Locate every blood parasite and identify its species.
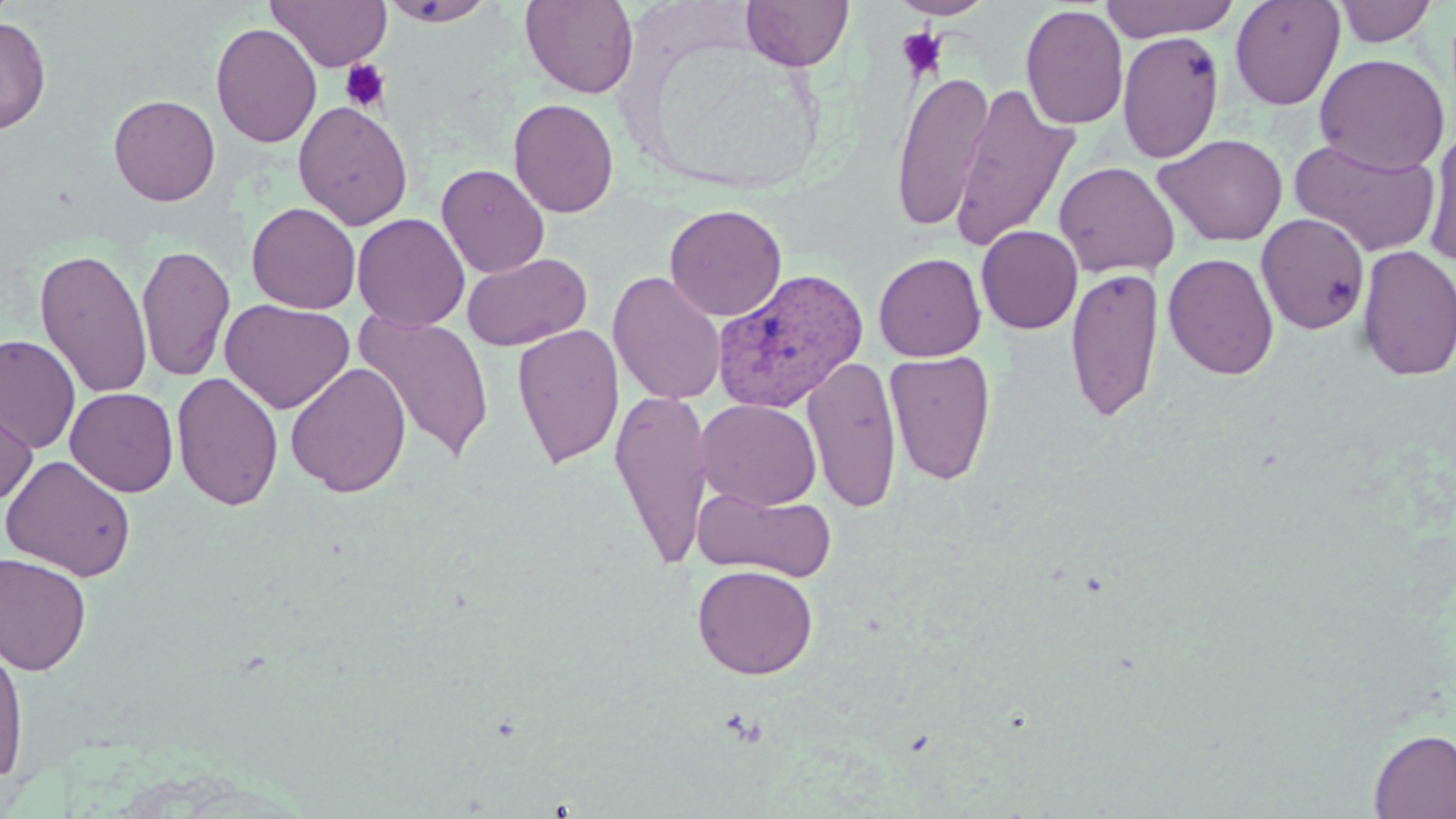

Approximate bounding boxes as (x1, y1, x2, y2) in pixels.
Plasmodium vivax-infected red blood cells: (713, 268, 869, 413).
No Plasmodium falciparum, Plasmodium ovale, Plasmodium malariae, Babesia divergens, or Trypanosoma brucei observed.

Summary:
  - Platelet locations: (897, 28, 947, 80), (339, 59, 390, 113)
  - Uninfected red blood cell locations: (378, 0, 497, 26), (520, 0, 639, 98), (741, 0, 853, 71), (890, 0, 995, 20), (1099, 0, 1241, 42), (1230, 0, 1345, 110), (1333, 0, 1439, 47), (267, 1, 391, 71), (1020, 4, 1129, 130), (0, 15, 51, 135), (210, 22, 322, 148), (1116, 30, 1225, 164), (1314, 53, 1450, 175), (890, 70, 994, 231), (948, 83, 1080, 251), (108, 94, 221, 206), (508, 98, 619, 218), (293, 100, 413, 231), (1422, 128, 1456, 266), (1153, 132, 1288, 246), (1289, 137, 1442, 257), (1054, 160, 1180, 278), (436, 163, 550, 279), (246, 202, 361, 314), (665, 204, 786, 321), (352, 213, 470, 331), (1256, 213, 1370, 335), (976, 225, 1083, 334), (136, 245, 236, 381), (1355, 246, 1456, 381), (35, 247, 152, 399), (462, 252, 592, 351), (873, 252, 986, 361), (1163, 253, 1279, 380), (1064, 266, 1164, 424), (607, 270, 727, 405), (220, 298, 355, 413), (353, 311, 494, 464), (512, 323, 624, 469), (0, 335, 81, 453), (884, 350, 997, 486), (803, 355, 903, 513), (285, 361, 412, 498), (172, 372, 285, 511), (65, 387, 179, 496), (610, 388, 712, 570), (1, 389, 38, 505), (697, 399, 822, 510), (1, 454, 137, 581), (693, 485, 836, 583), (0, 552, 92, 675), (692, 564, 818, 679), (0, 640, 29, 786), (1368, 728, 1456, 818)
  - Slide-level diagnosis: Plasmodium vivax
  - Stain: May-Grünwald-Giemsa
  - Field of view: single
  - Modality: light microscopy
  - Magnification: 1000x
  - Image size: 1456×819 pixels
  - Preparation: thin blood film